Comment on the morphology of the erythrocytes.
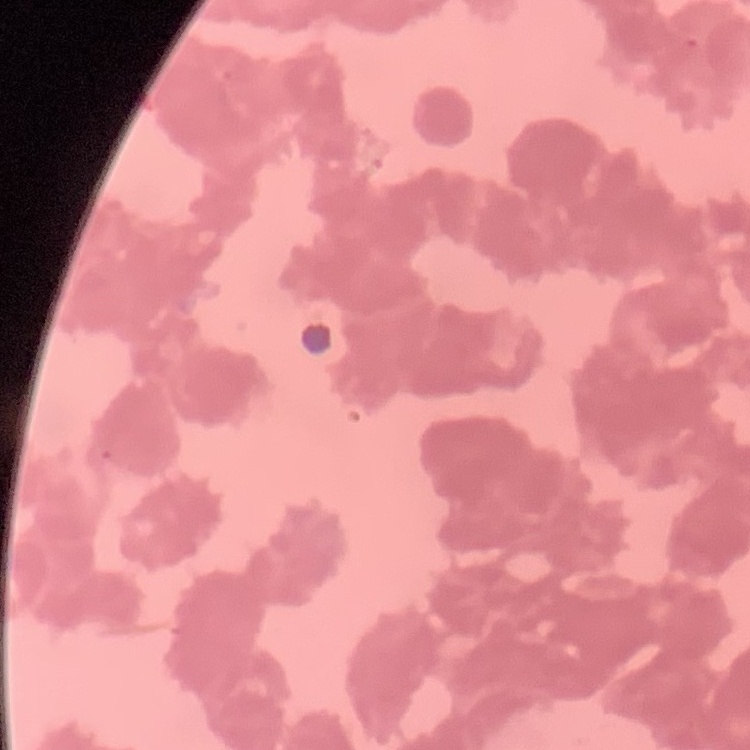
Rouleaux formation.

Summary:
  - Stain: Field's or Giemsa
  - Preparation: thin blood smear
  - Image type: square crop of a larger photomicrograph